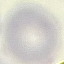
malaria status = uninfected
image type = automatically extracted cell patch, resized to 64 × 64 pixels
preparation = thin blood smear
stain = Giemsa
capture = smartphone through the microscope eyepiece